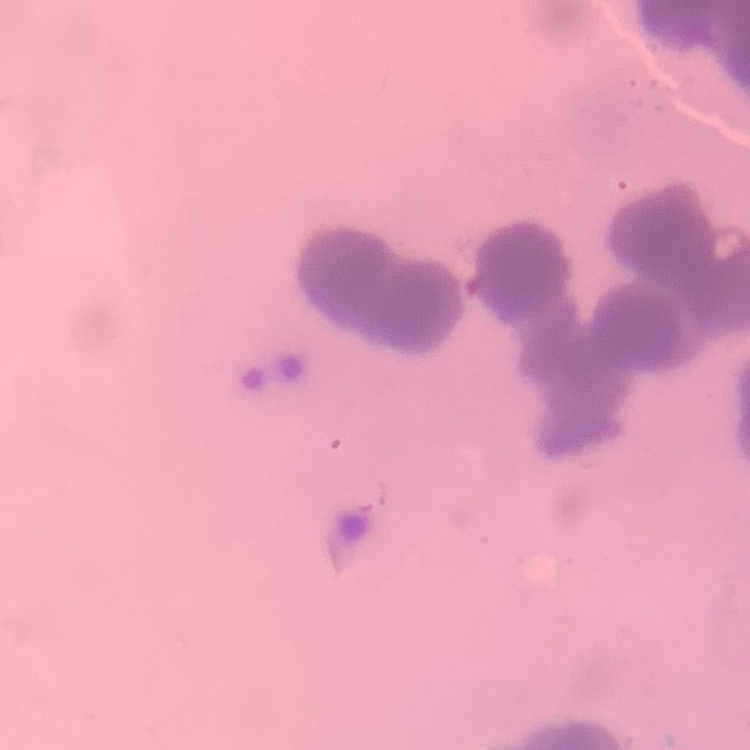
{
  "red_blood_cell_morphology": "rouleaux formation",
  "image_type": "one tile cut from a larger photomicrograph",
  "stain": "Field's or Giemsa",
  "preparation": "thin peripheral smear"
}